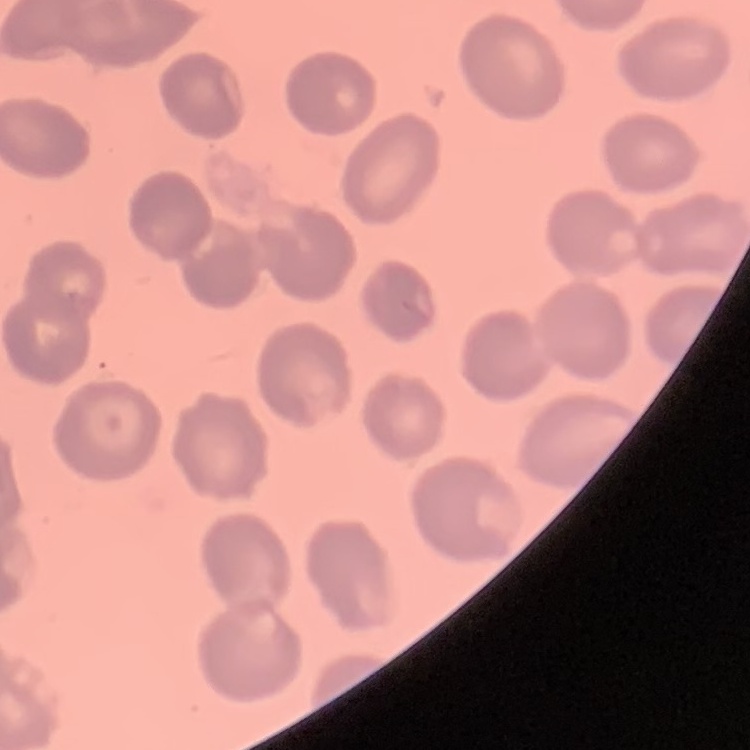

Summary:
  - Red blood cell morphology: no rouleaux formation
  - Preparation: thin blood film
  - Image type: one tile cut from a larger photomicrograph
  - Stain: Field's or Giemsa